Locate and identify every blood parasite.
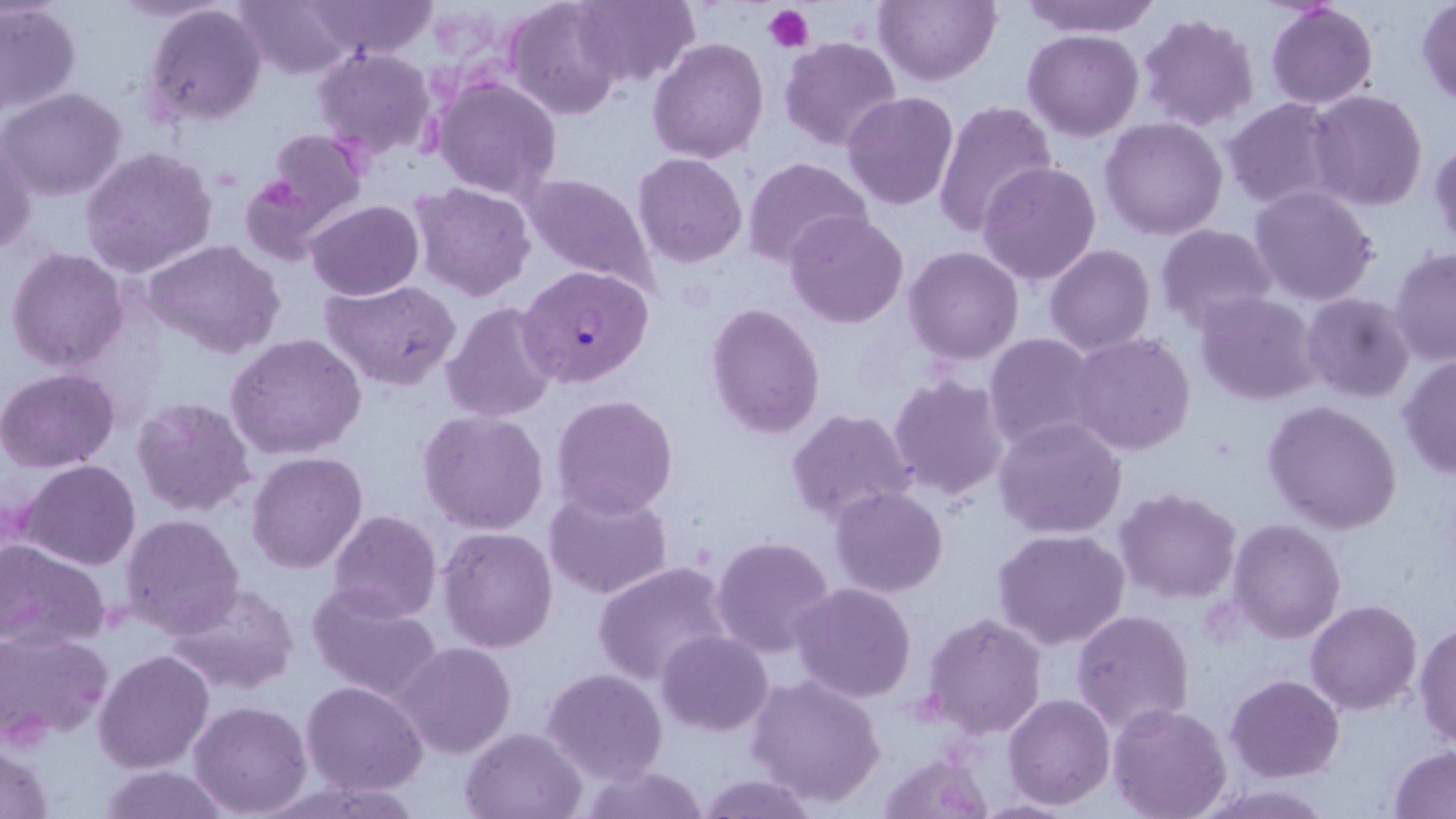
Approximate bounding boxes as named x1/y1/x2/y2 corners in pixels.
Plasmodium falciparum-infected red blood cells: (x1=519, y1=265, x2=655, y2=387).
No Plasmodium ovale, Plasmodium malariae, Plasmodium vivax, Babesia divergens, or Trypanosoma brucei observed.

Platelet locations: (x1=764, y1=4, x2=813, y2=53). Uninfected red blood cell locations: (x1=233, y1=0, x2=359, y2=79), (x1=571, y1=0, x2=699, y2=88), (x1=874, y1=0, x2=1001, y2=85), (x1=1016, y1=0, x2=1164, y2=36), (x1=306, y1=1, x2=440, y2=61), (x1=505, y1=1, x2=625, y2=118), (x1=1265, y1=2, x2=1377, y2=109), (x1=1414, y1=2, x2=1456, y2=108), (x1=0, y1=3, x2=82, y2=116), (x1=142, y1=3, x2=268, y2=128), (x1=1137, y1=13, x2=1259, y2=132), (x1=1024, y1=30, x2=1144, y2=141), (x1=647, y1=37, x2=769, y2=164), (x1=779, y1=37, x2=903, y2=153), (x1=312, y1=47, x2=437, y2=162), (x1=433, y1=77, x2=563, y2=202), (x1=1, y1=86, x2=129, y2=202), (x1=1308, y1=89, x2=1430, y2=211), (x1=842, y1=91, x2=959, y2=210), (x1=1223, y1=96, x2=1348, y2=210), (x1=932, y1=99, x2=1059, y2=238), (x1=1099, y1=117, x2=1229, y2=239), (x1=256, y1=127, x2=368, y2=241), (x1=1, y1=138, x2=38, y2=257), (x1=1430, y1=138, x2=1456, y2=253), (x1=80, y1=145, x2=218, y2=276), (x1=633, y1=153, x2=747, y2=267), (x1=743, y1=156, x2=874, y2=271), (x1=977, y1=161, x2=1101, y2=284), (x1=517, y1=170, x2=663, y2=300), (x1=239, y1=173, x2=332, y2=263), (x1=408, y1=182, x2=538, y2=302), (x1=420, y1=184, x2=543, y2=423), (x1=1247, y1=186, x2=1379, y2=307), (x1=306, y1=200, x2=423, y2=300), (x1=785, y1=210, x2=909, y2=328), (x1=1153, y1=224, x2=1278, y2=333), (x1=141, y1=239, x2=286, y2=361), (x1=1044, y1=244, x2=1155, y2=354), (x1=903, y1=245, x2=1025, y2=364), (x1=6, y1=246, x2=128, y2=374), (x1=1388, y1=246, x2=1455, y2=366), (x1=320, y1=278, x2=461, y2=390), (x1=1193, y1=291, x2=1322, y2=405), (x1=1302, y1=292, x2=1415, y2=404), (x1=441, y1=302, x2=561, y2=423), (x1=705, y1=302, x2=826, y2=439), (x1=1069, y1=332, x2=1197, y2=457), (x1=984, y1=333, x2=1105, y2=451), (x1=227, y1=334, x2=368, y2=460), (x1=1398, y1=354, x2=1456, y2=480), (x1=0, y1=368, x2=121, y2=472), (x1=886, y1=372, x2=1011, y2=503), (x1=550, y1=393, x2=679, y2=520), (x1=131, y1=395, x2=257, y2=517), (x1=1263, y1=400, x2=1403, y2=535), (x1=786, y1=408, x2=918, y2=525), (x1=417, y1=409, x2=551, y2=535), (x1=992, y1=415, x2=1128, y2=539), (x1=245, y1=451, x2=368, y2=574), (x1=19, y1=460, x2=140, y2=569), (x1=544, y1=484, x2=674, y2=600), (x1=829, y1=486, x2=948, y2=598), (x1=1114, y1=489, x2=1241, y2=604), (x1=327, y1=510, x2=441, y2=624), (x1=121, y1=514, x2=245, y2=636), (x1=1228, y1=519, x2=1345, y2=643), (x1=438, y1=527, x2=559, y2=653), (x1=992, y1=527, x2=1132, y2=648), (x1=711, y1=535, x2=837, y2=658), (x1=0, y1=539, x2=108, y2=649), (x1=592, y1=560, x2=738, y2=687), (x1=162, y1=581, x2=302, y2=695), (x1=307, y1=582, x2=444, y2=704), (x1=790, y1=582, x2=918, y2=702), (x1=1305, y1=601, x2=1423, y2=716), (x1=1071, y1=609, x2=1196, y2=737), (x1=922, y1=612, x2=1048, y2=738), (x1=1413, y1=620, x2=1456, y2=749), (x1=1, y1=630, x2=114, y2=744), (x1=657, y1=631, x2=773, y2=736), (x1=395, y1=642, x2=517, y2=758), (x1=94, y1=649, x2=214, y2=772), (x1=540, y1=668, x2=668, y2=783), (x1=746, y1=673, x2=887, y2=808), (x1=1226, y1=674, x2=1344, y2=781), (x1=300, y1=680, x2=429, y2=798), (x1=1003, y1=693, x2=1115, y2=810), (x1=188, y1=700, x2=313, y2=817), (x1=1106, y1=702, x2=1232, y2=819), (x1=459, y1=726, x2=587, y2=818), (x1=1, y1=743, x2=54, y2=819), (x1=1389, y1=745, x2=1456, y2=817), (x1=875, y1=748, x2=993, y2=818), (x1=95, y1=763, x2=231, y2=819), (x1=576, y1=763, x2=708, y2=819), (x1=694, y1=773, x2=823, y2=819), (x1=1194, y1=781, x2=1336, y2=817). Slide-level diagnosis: Plasmodium falciparum. May-Grünwald-Giemsa stain. Image is 1456×819 pixels. Thin blood film. 1000x magnification. Single field of view. Light microscopy.